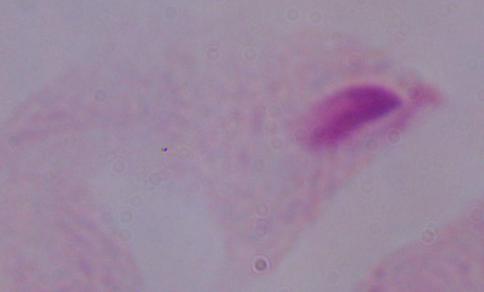
magnification = 1000x
identification = trichomonad
modality = micrograph